Locate every Plasmodium falciparum-infected red blood cell.
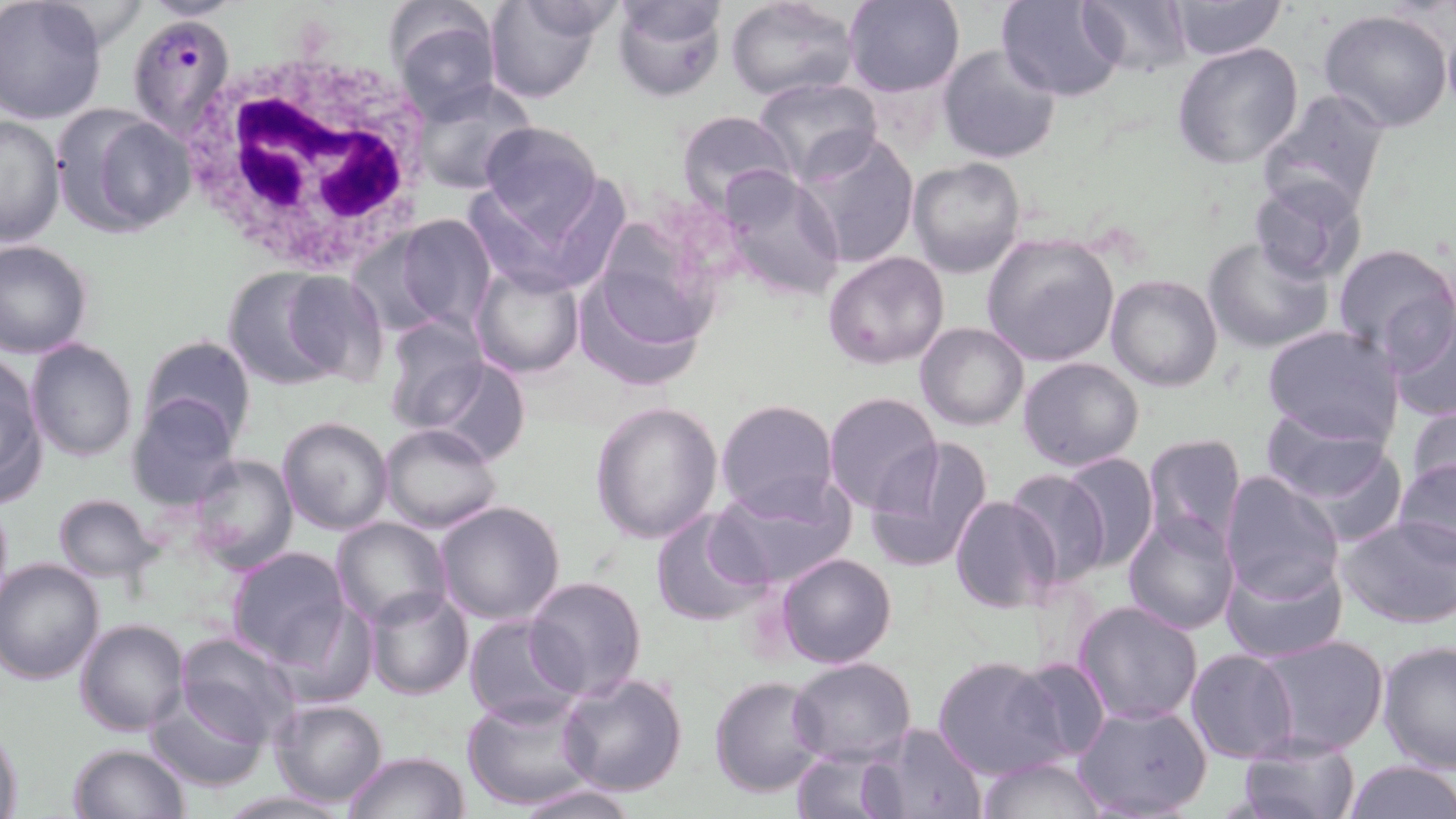

Approximate bounding boxes as (x1,y1)-(x2,y2) corner pairs in pixels.
Plasmodium falciparum-infected red blood cells: (127,10)-(235,140).

White blood cell locations: (172,45)-(439,274). Uninfected red blood cell locations: (483,0)-(606,104), (612,0)-(728,102), (842,0)-(965,97), (998,0)-(1128,101), (1080,0)-(1191,78), (1168,0)-(1287,62), (725,1)-(858,101), (0,2)-(108,126), (384,4)-(504,117), (1318,7)-(1455,133), (1443,19)-(1456,118), (1172,41)-(1305,170), (937,43)-(1061,164), (753,77)-(883,185), (409,79)-(537,196), (1257,90)-(1390,219), (54,110)-(191,237), (677,110)-(798,220), (0,111)-(64,249), (478,119)-(604,235), (796,130)-(919,269), (908,158)-(1028,278), (717,167)-(848,302), (1249,177)-(1367,286), (391,213)-(497,335), (588,219)-(723,349), (980,232)-(1120,367), (1202,235)-(1332,353), (0,240)-(94,358), (1330,244)-(1456,363), (822,250)-(949,369), (470,263)-(585,380), (576,267)-(708,393), (220,268)-(347,391), (282,272)-(390,388), (1105,275)-(1223,391), (1385,299)-(1456,420), (380,315)-(489,432), (917,323)-(1029,431), (1262,325)-(1404,447), (140,335)-(256,444), (26,339)-(137,462), (1,353)-(46,503), (1018,356)-(1144,472), (426,358)-(530,467), (127,391)-(244,510), (824,392)-(942,512), (714,397)-(838,520), (1403,399)-(1455,502), (590,400)-(724,544), (1262,406)-(1391,505), (135,416)-(282,552), (277,416)-(393,534), (379,423)-(502,534), (1140,433)-(1248,548), (865,436)-(994,574), (1276,436)-(1413,547), (1057,451)-(1159,571), (185,454)-(298,574), (1393,455)-(1455,565), (1005,467)-(1110,589), (1219,470)-(1344,601), (717,473)-(857,587), (52,493)-(162,583), (950,494)-(1063,613), (0,499)-(12,610), (434,500)-(567,625), (650,508)-(770,628), (1123,512)-(1241,636), (1336,515)-(1456,628), (330,517)-(453,629), (225,547)-(351,667), (1219,551)-(1348,661), (775,552)-(897,670), (1,558)-(106,684), (524,575)-(647,701), (364,587)-(473,701), (1072,599)-(1205,725), (464,614)-(582,728), (75,618)-(190,735), (174,630)-(298,745), (1258,635)-(1389,755), (1376,640)-(1456,774), (1185,649)-(1299,764), (787,655)-(916,767), (933,655)-(1063,781), (1011,656)-(1113,762), (557,670)-(689,796), (707,675)-(827,799), (145,688)-(270,791), (462,693)-(600,812), (269,697)-(390,807), (1072,701)-(1212,819), (83,713)-(257,809), (0,720)-(22,819), (864,722)-(990,819), (1237,733)-(1361,819), (68,743)-(189,819), (790,749)-(900,819), (342,750)-(471,818), (977,756)-(1108,818), (1339,759)-(1455,819), (509,782)-(639,818). Slide-level diagnosis: Plasmodium falciparum. One field of a larger specimen. Thin blood smear. Light microscopy. Image is 1456×819 pixels. May-Grünwald-Giemsa-stained preparation. 1000x magnification.